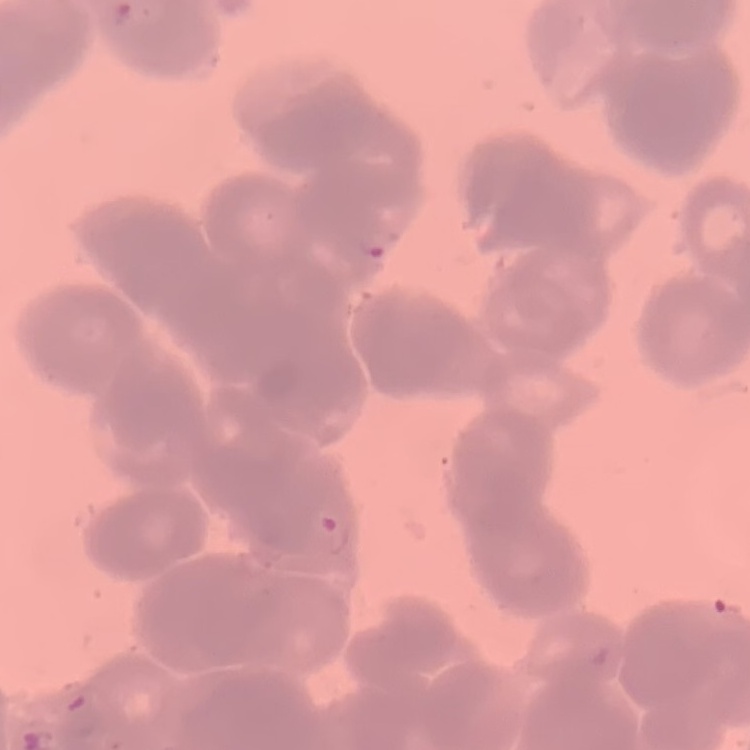
Summary:
  - Red blood cell morphology: rouleaux formation
  - Preparation: thin blood film
  - Stain: Field's or Giemsa
  - Image type: square crop of a larger photomicrograph